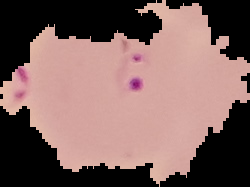 Cell region segmented out of the field of view; the surrounding area is masked to black. Image is 250×187 pixels. From a thin blood film. Malaria status: parasitized.